State the preparation type.
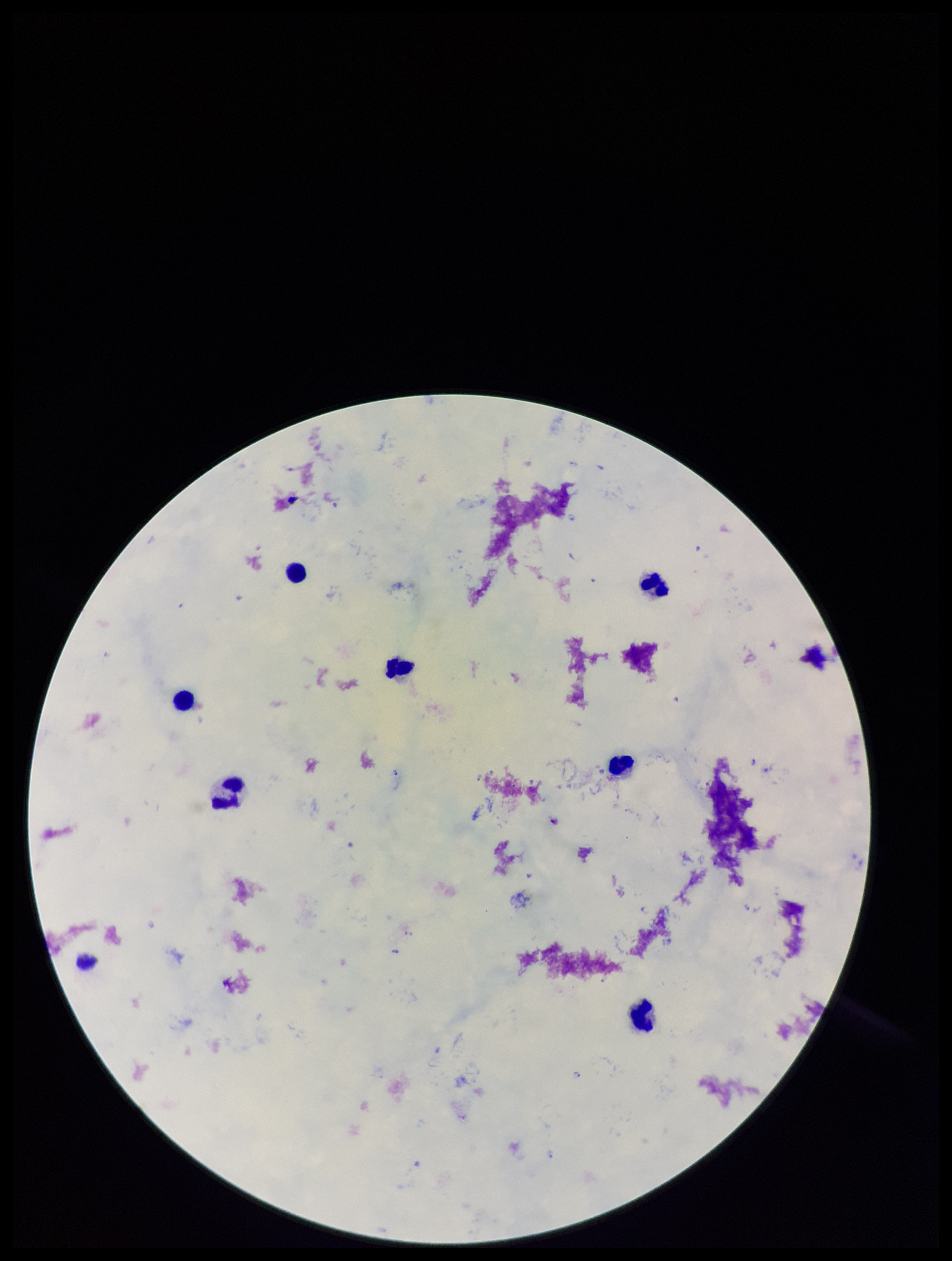

Thick.

Summary:
  - Stain: Giemsa
  - Field of view: one from this slide
  - Plasmodium parasites: detected
  - Patient malaria status: positive
  - Capture: smartphone photograph through the microscope eyepiece
  - Parasite count: 7
  - Leukocyte count: 9
  - Image size: 952×1261 pixels
  - Species reported for this patient: Plasmodium falciparum